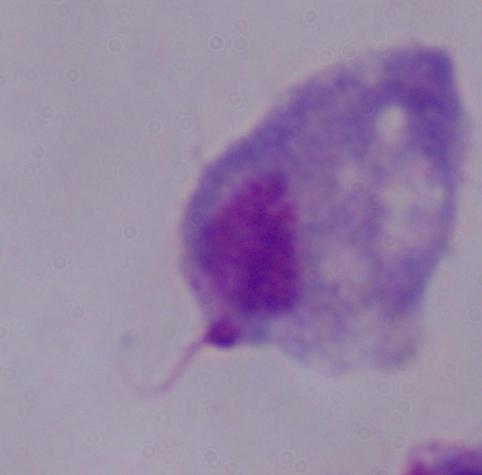

identification: trichomonad
magnification: 1000x
modality: micrograph